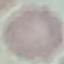 Result: negative for malaria parasites. Cell patch, automatically extracted from a larger field of view and resized to 64 × 64 pixels. Giemsa-stained preparation. Thin smear of blood. Acquired by smartphone through the microscope eyepiece.